Comment on the morphology of the erythrocytes.
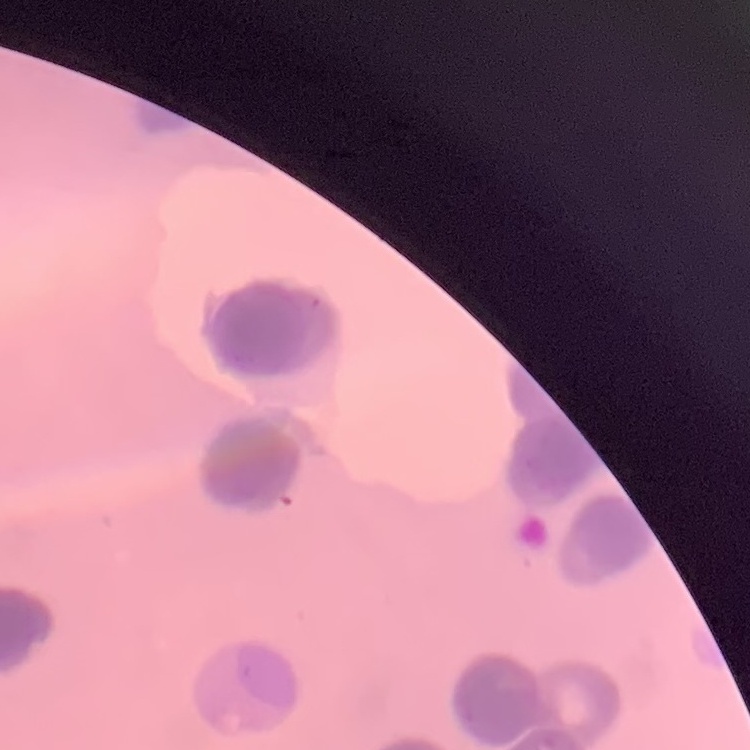

Rouleaux formation.

Stained with either Field's or Giemsa. One tile cut from a larger photomicrograph. Thin blood smear.